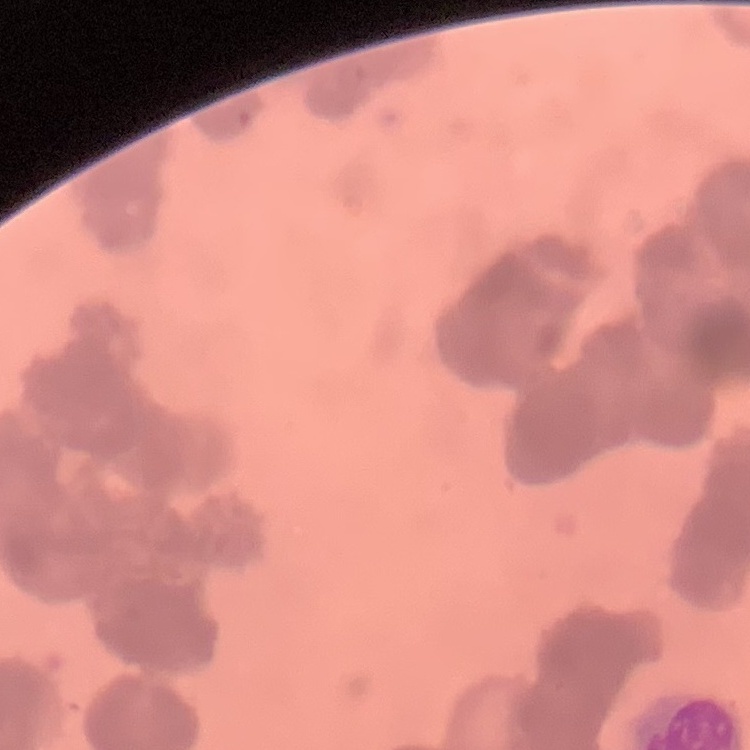
The red blood cells show rouleaux formation. Stained with either Field's or Giemsa. Thin blood smear. One tile cut from a larger photomicrograph.